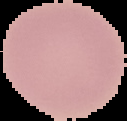

The area outside the segmented cell region is set to black. From a thin blood film. Result: no Plasmodium parasites detected. Image is 127×121 pixels.